Classify this cell by malaria status.
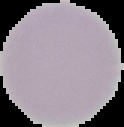

It is uninfected.

Image is 124×127 pixels. Segmented cell region on a black background. From a thin blood smear.